Report the malaria status of this cell.
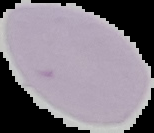
It is uninfected.

image type = segmented cell region on a black background
preparation = thin blood smear
image size = 154×133 pixels